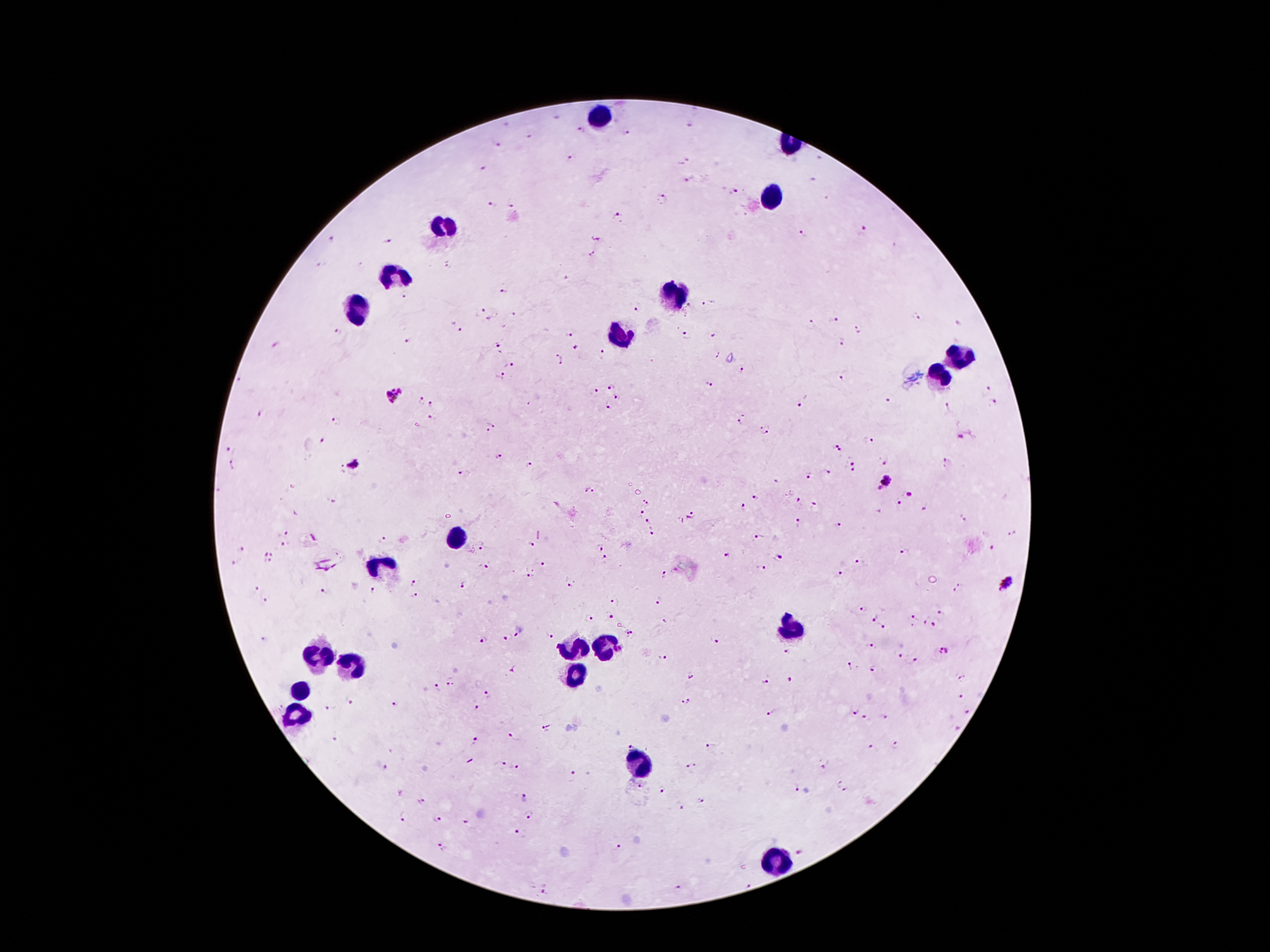
Approximate centers as (x, y) in pixels. Malaria parasite locations: (557, 118), (508, 126), (692, 127), (579, 130), (626, 131), (530, 135), (498, 144), (570, 158), (683, 162), (481, 167), (690, 181), (734, 192), (663, 197), (488, 203), (511, 203), (618, 215), (864, 231), (804, 236), (389, 240), (333, 241), (592, 252), (323, 263), (448, 264), (506, 290), (406, 297), (710, 304), (689, 306), (636, 309), (480, 311), (514, 313), (917, 316), (834, 318), (813, 321), (958, 323), (859, 328), (460, 330), (339, 331), (568, 332), (687, 335), (715, 335), (409, 341), (501, 343), (842, 344), (276, 346), (576, 347), (603, 354), (715, 354), (559, 359), (511, 365), (743, 370), (502, 376), (843, 380), (611, 385), (709, 385), (986, 389), (595, 392), (394, 396), (617, 397), (889, 400), (419, 402), (800, 403), (433, 405), (994, 405), (948, 407), (607, 408), (260, 415), (432, 418), (744, 418), (336, 423), (491, 427), (765, 430), (960, 437), (323, 440), (868, 440), (835, 443), (231, 449), (839, 452), (500, 457), (854, 459), (886, 460), (947, 462), (232, 463), (353, 465), (530, 465), (850, 469), (342, 470), (827, 473), (464, 474), (809, 475), (776, 480), (883, 482), (218, 489), (590, 490), (910, 493), (755, 496), (799, 500), (332, 502), (900, 502), (650, 503), (816, 505), (927, 506), (744, 508), (640, 513), (294, 514), (691, 515), (963, 518), (648, 520), (798, 525), (838, 525), (1014, 532), (282, 534), (650, 535), (314, 536), (760, 537), (384, 540), (482, 544), (530, 544), (285, 545), (598, 547), (241, 548), (992, 549), (269, 550), (905, 552), (728, 555), (780, 556), (606, 560), (268, 562), (860, 563), (235, 564), (483, 565), (545, 565), (759, 569), (839, 573), (662, 574), (528, 576), (570, 581), (961, 582), (414, 584), (466, 585), (1006, 585), (255, 590), (373, 591), (326, 592), (955, 592), (417, 595), (267, 598), (616, 599), (659, 600), (861, 609), (943, 610), (610, 615), (872, 616), (915, 617), (588, 618), (927, 618), (665, 621), (936, 623), (881, 626), (634, 632), (623, 633), (517, 637), (550, 638), (263, 639), (485, 640), (506, 640), (713, 641), (868, 645), (943, 651), (789, 652), (899, 655), (662, 656), (915, 661), (848, 667), (871, 669), (514, 671), (693, 676), (961, 678), (791, 679), (451, 680), (766, 682), (439, 688), (489, 695), (959, 697), (349, 701), (685, 701), (394, 705), (478, 706), (330, 708), (856, 709), (967, 710), (771, 712), (866, 718), (884, 719), (547, 726), (956, 727), (336, 736), (512, 738), (475, 742), (631, 743), (893, 746), (710, 747), (872, 747), (500, 763), (692, 766), (823, 767), (382, 768), (516, 768), (571, 775), (839, 783), (641, 785), (796, 787), (663, 790), (847, 792), (525, 798), (424, 801), (701, 801), (682, 807), (403, 815), (530, 815), (437, 820), (465, 822), (519, 832), (443, 845), (618, 849), (799, 852), (750, 882), (546, 888), (675, 888). Leukocyte locations: (600, 115), (772, 195), (442, 224), (394, 277), (673, 291), (356, 306), (619, 337), (956, 355), (938, 378), (457, 538), (383, 569), (789, 629), (570, 648), (606, 650), (316, 657), (350, 665), (576, 671), (300, 690), (295, 718), (640, 762), (780, 857). Photographed through the microscope eyepiece with a smartphone camera. 100x magnification. Thick blood smear. Giemsa stain. Single field of view. Image is 1270×952 pixels. Patient malaria status: positive for Plasmodium falciparum.